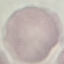
Summary:
  - Malaria status: uninfected
  - Image type: automatically extracted cell patch, resized to 64 × 64 pixels
  - Preparation: thin blood smear
  - Stain: Giemsa
  - Capture: smartphone through the microscope eyepiece